Assess this cell for malaria.
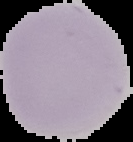

Uninfected.

preparation = thin blood smear
image size = 133×142 pixels
image type = segmented cell region on a black background